State which cell type is depicted.
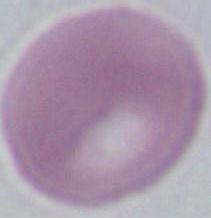

This is an erythrocyte.

Micrograph. Captured at 1000x magnification.